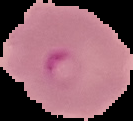 From a thin blood smear. The area outside the segmented cell region is set to black. Malaria status: parasitized. Image is 133×121 pixels.